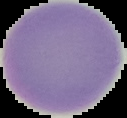 From a thin blood smear. Cell region segmented out of the field of view; the surrounding area is masked to black. Malaria status: uninfected. Image is 127×118 pixels.